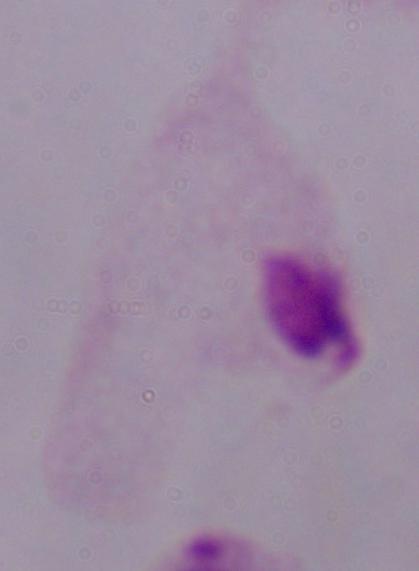 1000x magnification. A trichomonad is seen. Photomicrograph.